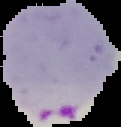

image type = segmented cell region with the area outside set to black
result = Plasmodium parasites identified
preparation = thin blood smear
image size = 121×127 pixels